Point out each leukocyte.
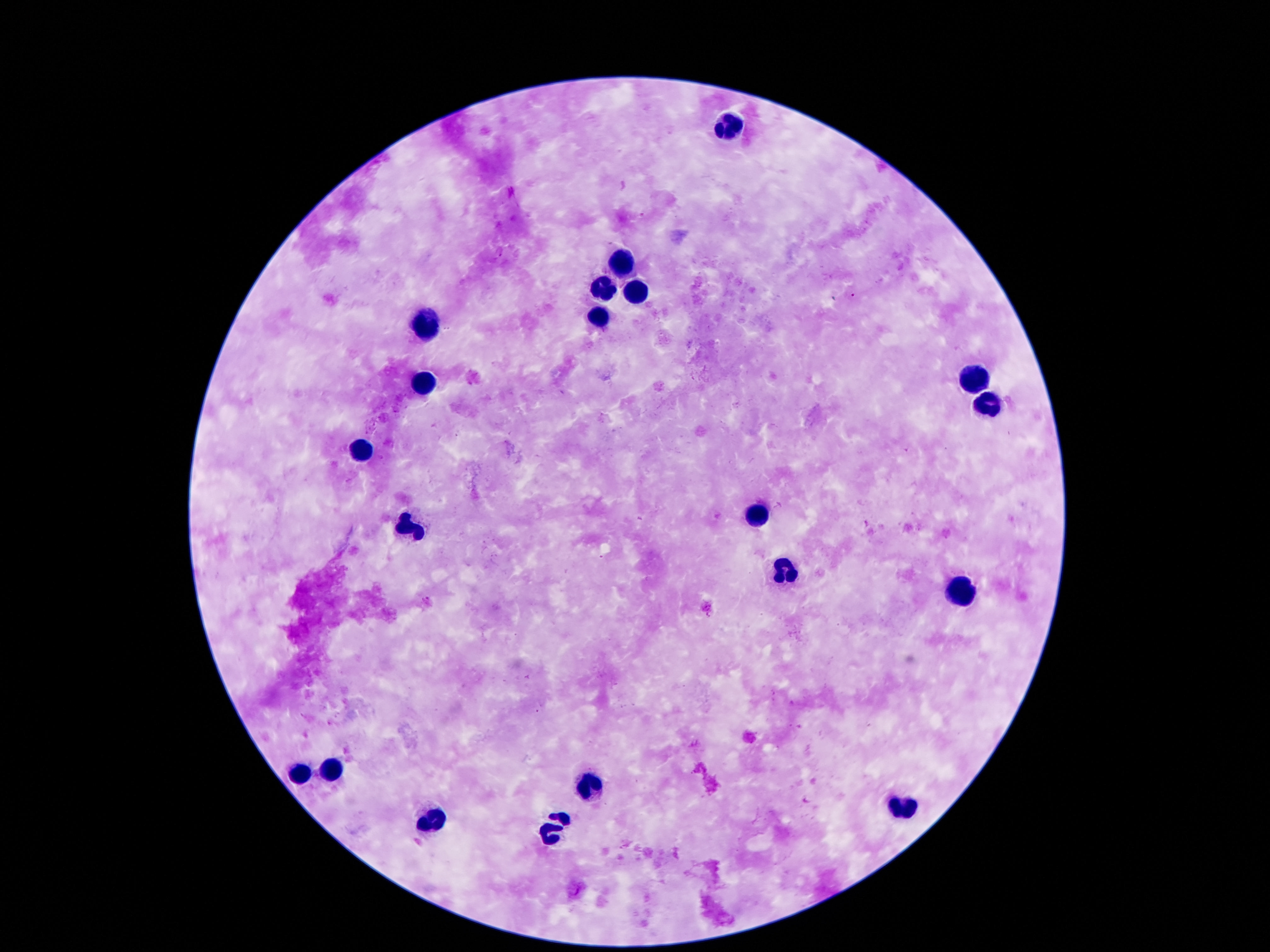

Approximate centers as {x, y} in pixels.
Leukocytes: {727, 121}, {618, 261}, {604, 287}, {639, 294}, {598, 316}, {424, 324}, {971, 379}, {424, 383}, {987, 408}, {360, 455}, {754, 514}, {409, 529}, {786, 570}, {965, 593}, {329, 771}, {299, 775}, {585, 785}, {901, 805}, {426, 819}, {553, 830}.

capture = smartphone camera through the microscope eyepiece
image size = 1270×952 pixels
field of view = one from this slide
preparation = thick blood film
patient malaria status = negative
magnification = 100x
stain = Giemsa